Comment on the morphology of the red blood cells.
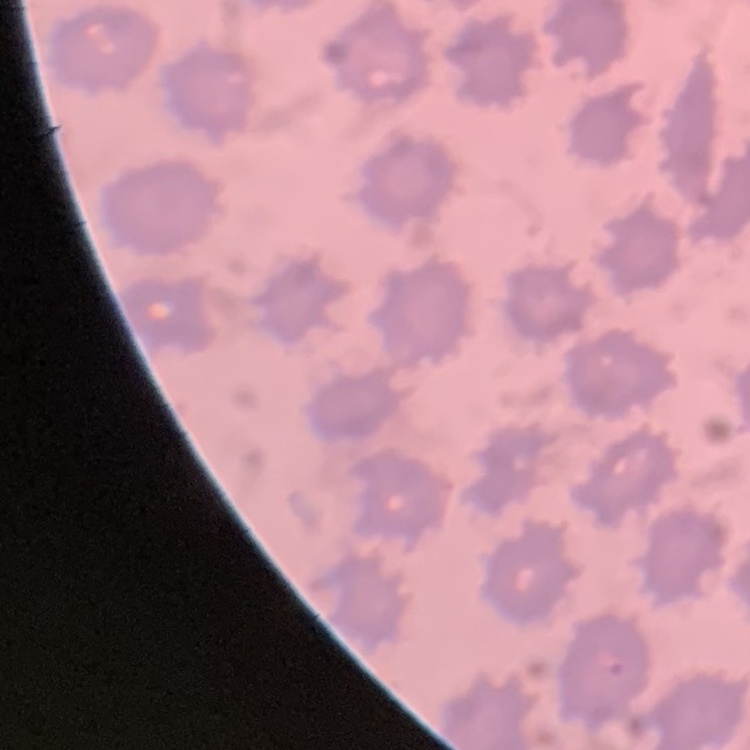

No rouleaux formation.

preparation = thin peripheral smear
image type = square crop of a larger photomicrograph
stain = Field's or Giemsa